Identify the preparation type.
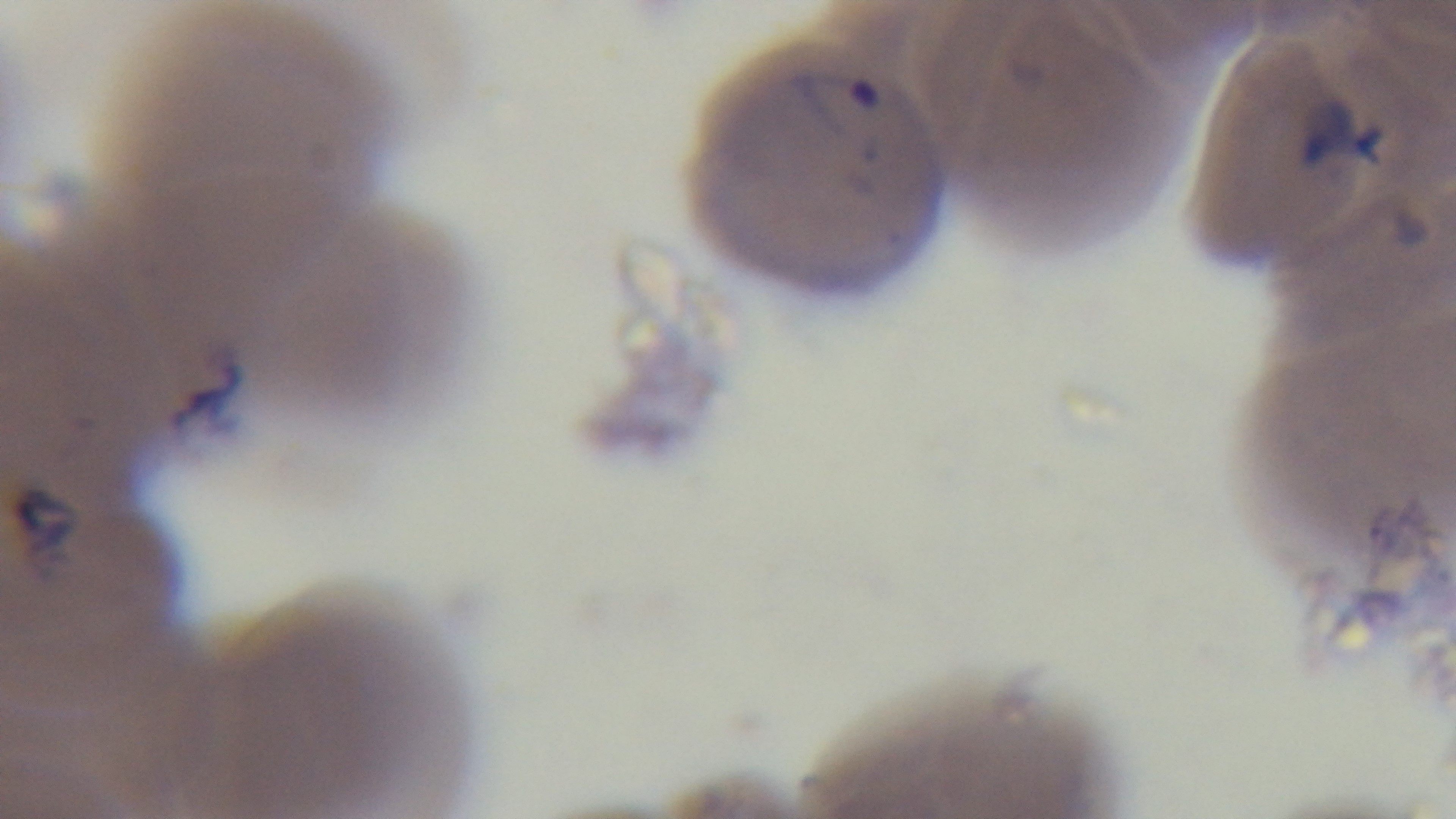

A thin smear.

Captured with a mounted 4K digital camera. Single field of view. Malaria status: infected. Giemsa-stained. Photomicrograph. Oil-immersion objective, 100x.